Comment on the morphology of the red blood cells.
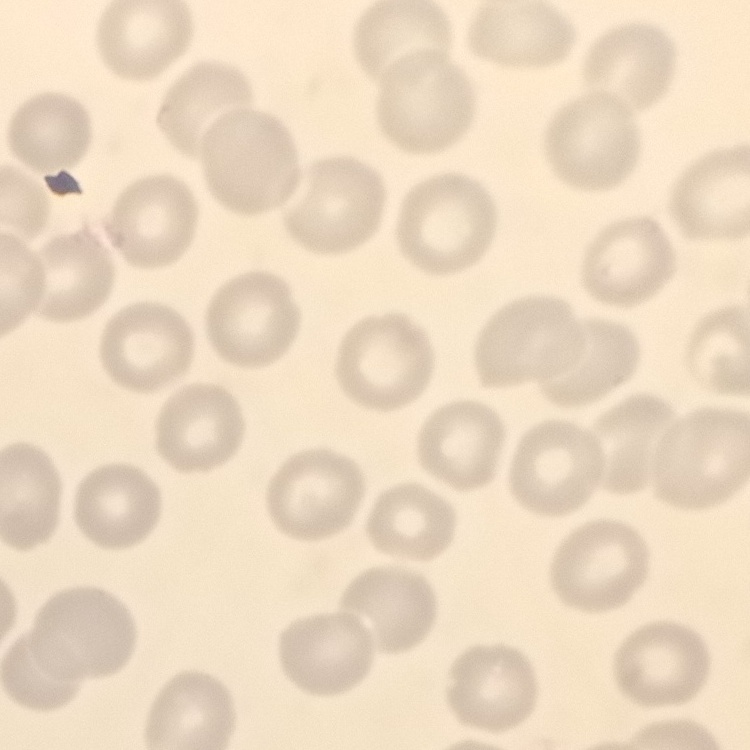

No rouleaux formation.

Summary:
  - Image type: square crop of a larger photomicrograph
  - Stain: Field's or Giemsa
  - Preparation: thin peripheral smear